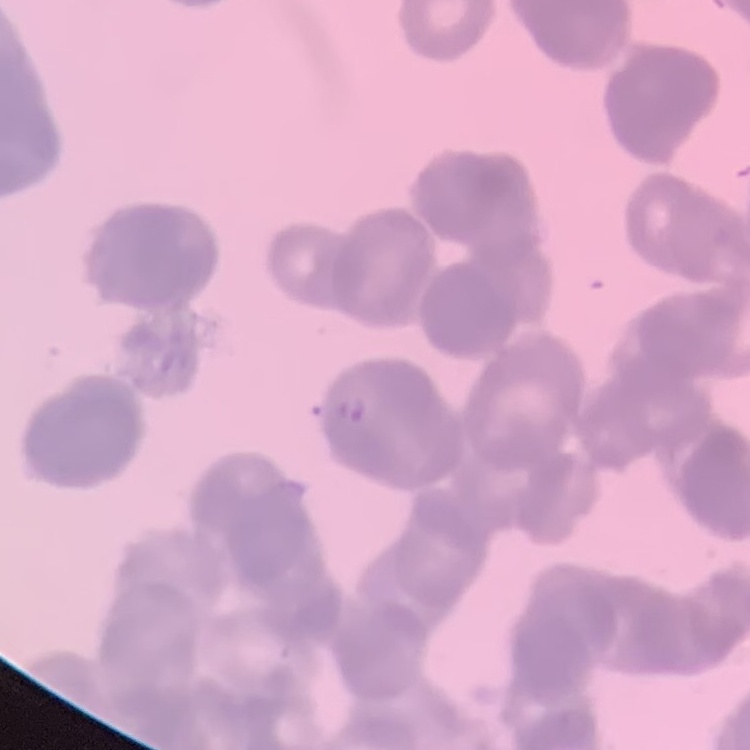

erythrocyte morphology = rouleaux formation
preparation = thin blood film
image type = square crop of a larger photomicrograph
stain = Field's or Giemsa